Report the malaria status of this cell.
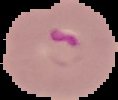
It is parasitized.

Summary:
  - Preparation: thin blood smear
  - Image type: segmented cell region with the area outside set to black
  - Image size: 118×100 pixels